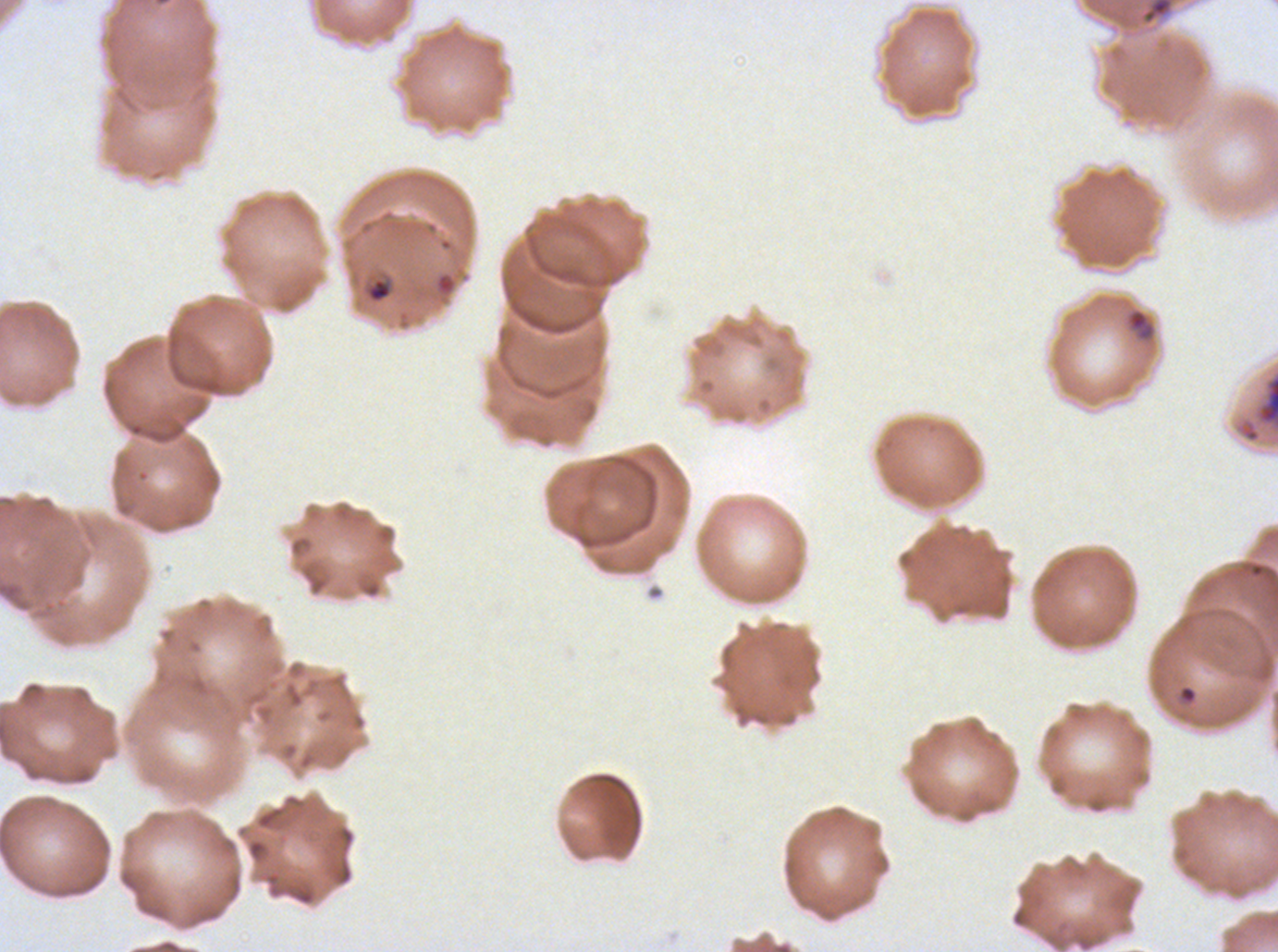 Approximate bounding rectangles given as corner coordinates in pixels from the top-left. Ring locations: (x1=1124, y1=307, x2=1157, y2=343), (x1=1178, y1=685, x2=1198, y2=704). Debris locations: (x1=1137, y1=0, x2=1175, y2=26). Late-ring/early-trophozoite locations: (x1=366, y1=277, x2=392, y2=303). Late schizont locations: (x1=1234, y1=369, x2=1277, y2=445). Life-cycle stages observed: ring, late-ring/early-trophozoite, late schizont. Giemsa-stained preparation. Image is 1278×952 pixels. P. falciparum cultured ex vivo for 24 to 48 hours, from a patient in The Gambia. A sub-image separated from a larger composite. Thin blood film.